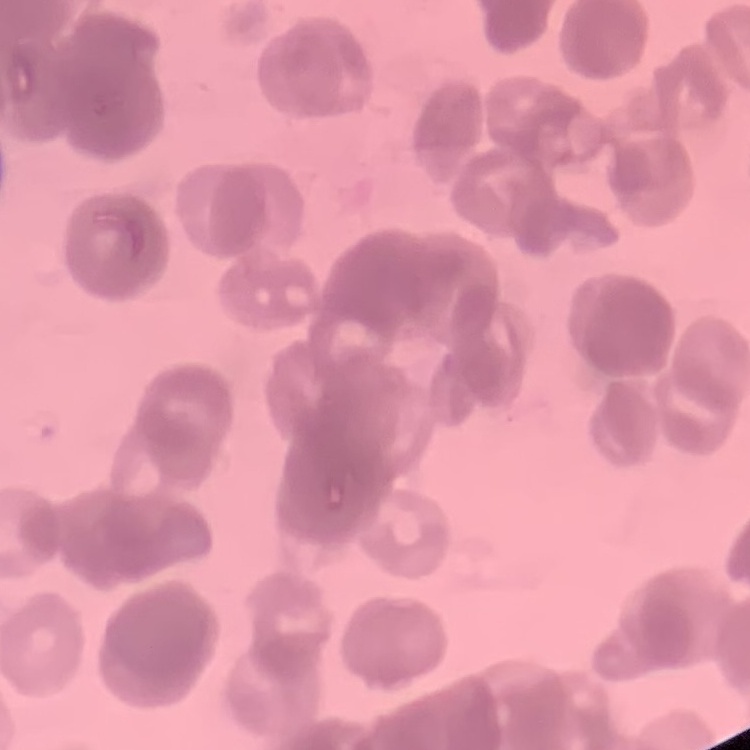
Summary:
  - Red blood cell morphology: rouleaux formation
  - Preparation: thin blood smear
  - Stain: Field's or Giemsa
  - Image type: square crop of a larger photomicrograph